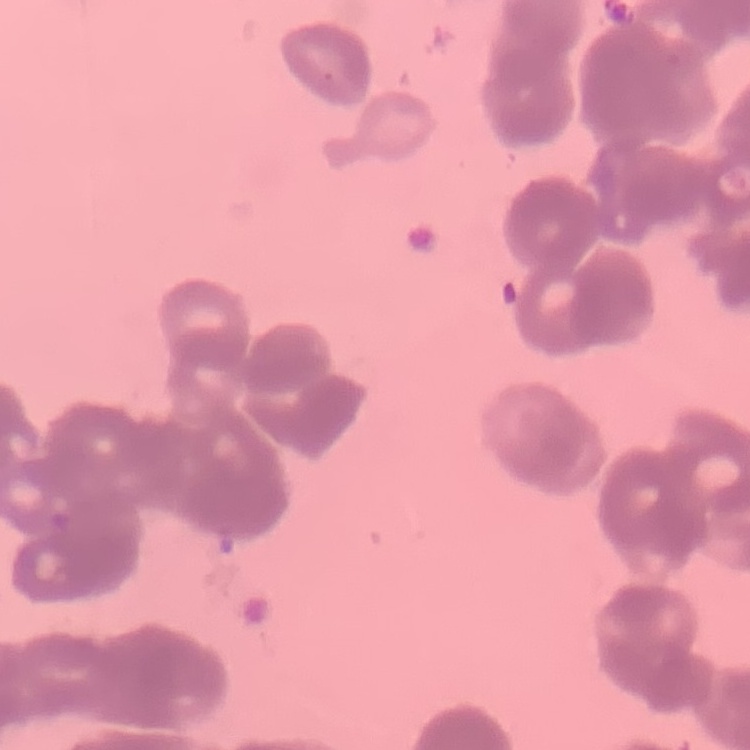

erythrocyte morphology = rouleaux formation
image type = square crop of a larger photomicrograph
preparation = thin blood film
stain = Field's or Giemsa